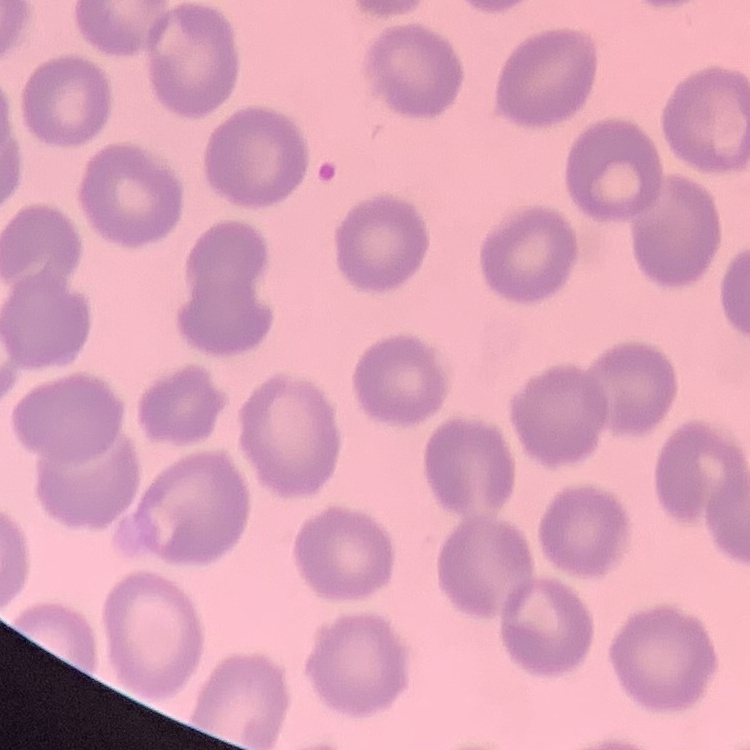

{
  "red_blood_cell_morphology": "no rouleaux formation",
  "stain": "Field's or Giemsa",
  "preparation": "thin blood film",
  "image_type": "square crop of a larger photomicrograph"
}